Classify this cell by malaria status.
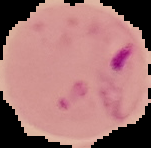
Parasitized.

Summary:
  - Image type: segmented cell region with the area outside set to black
  - Image size: 151×148 pixels
  - Preparation: thin blood film